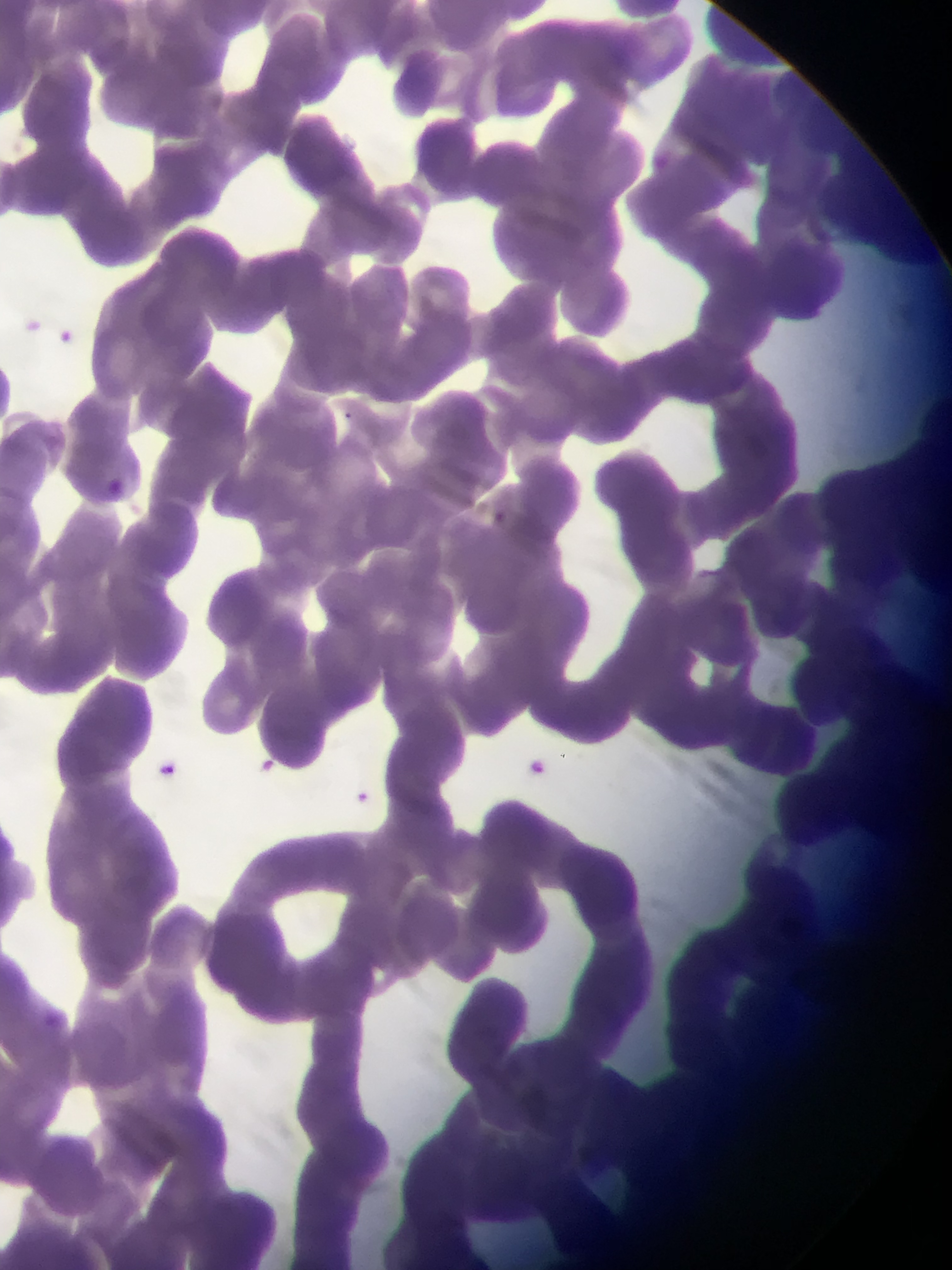
preparation = thin blood smear
field of view = single
country = Ghana
capture = mobile-phone photograph through a microscope
malaria parasite locations = approximate bounding boxes as {left, top, right, bottom} in pixels: {651, 149, 672, 170}, {22, 316, 45, 340}, {49, 327, 71, 349}, {342, 404, 365, 434}, {98, 480, 154, 510}, {487, 504, 510, 536}, {524, 753, 569, 793}, {153, 755, 176, 783}, {250, 755, 307, 786}, {351, 786, 385, 820}, {31, 1004, 95, 1040}
image size = 952×1270 pixels